Comment on the morphology of the red blood cells.
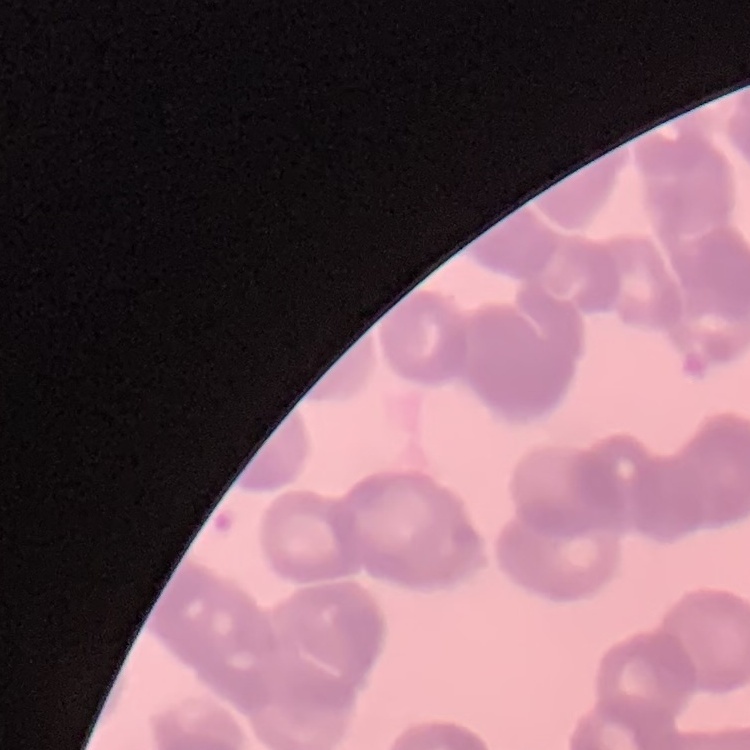
They show rouleaux formation.

stain = Field's or Giemsa
preparation = thin blood smear
image type = one tile cut from a larger photomicrograph